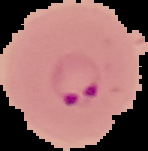

{
  "image_type": "segmented cell region with the area outside set to black",
  "result": "malaria parasites detected",
  "preparation": "thin blood smear",
  "image_size": "148×151 pixels"
}